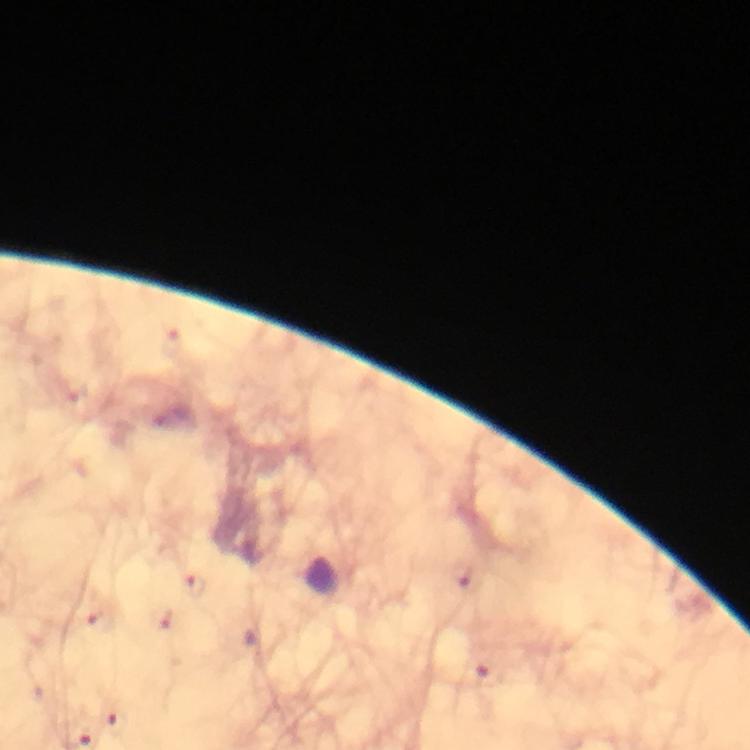

capture: smartphone camera through the microscope
magnification: 100x
immersion_oil: applied
image_size: 750×750 pixels
context: from a malaria diagnostic workup
cropped_from: a single field of view
preparation: thick blood smear
stain: Giemsa
malaria_parasite_locations: 'approximate centers as (x, y) in pixels: (195, 586), (117, 721)'